Assess this cell for malaria.
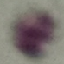

It is uninfected.

Thin blood smear. Photographed with a smartphone camera at the microscope eyepiece. Giemsa-stained preparation. Automatically extracted cell patch, resized to 64 × 64 pixels.